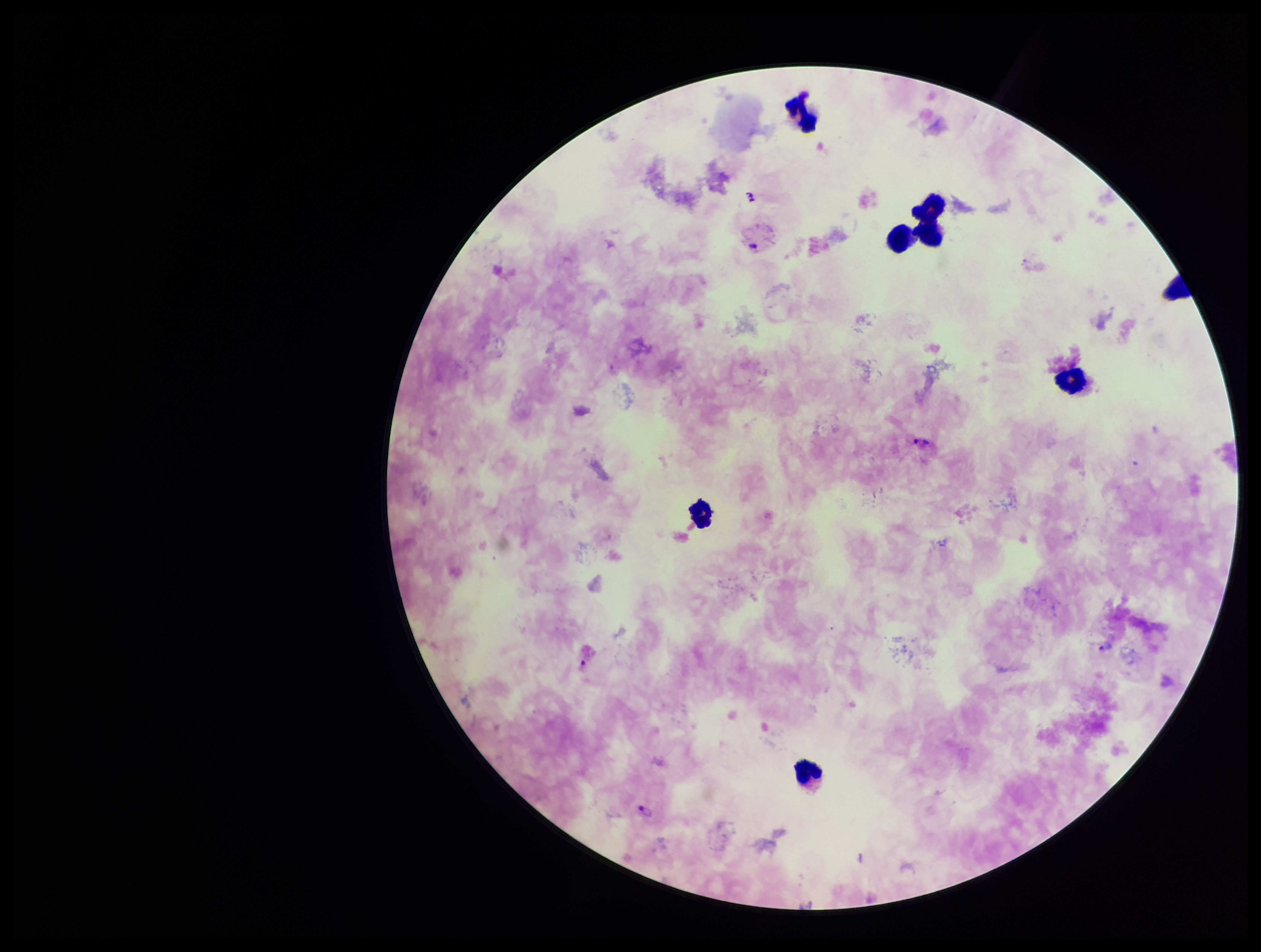
Summary:
  - Patient malaria status: infected
  - Leukocyte count: 7
  - Species reported for this patient: Plasmodium vivax
  - Parasite count: 4
  - Preparation: thick
  - Field of view: single
  - Image size: 1261×952 pixels
  - Stain: Giemsa
  - Capture: smartphone photograph through the microscope eyepiece
  - Plasmodium parasites: seen